Assess this cell for malaria.
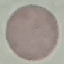
It is uninfected.

image type = cell patch, automatically extracted from a larger field of view and resized to 64 × 64 pixels
capture = smartphone camera at the microscope eyepiece
stain = Giemsa
preparation = thin blood film